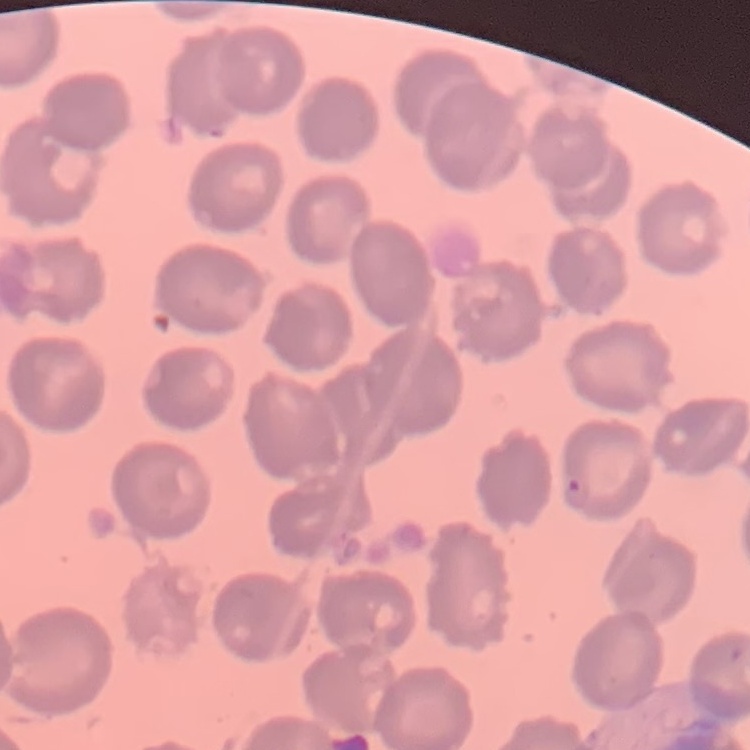
red blood cell morphology = no rouleaux formation
preparation = thin blood smear
stain = Field's or Giemsa
image type = one tile cut from a larger photomicrograph